Classify this cell by malaria status.
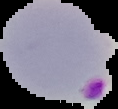

It is parasitized.

Summary:
  - Image size: 118×109 pixels
  - Image type: segmented cell region with the area outside set to black
  - Preparation: thin blood smear